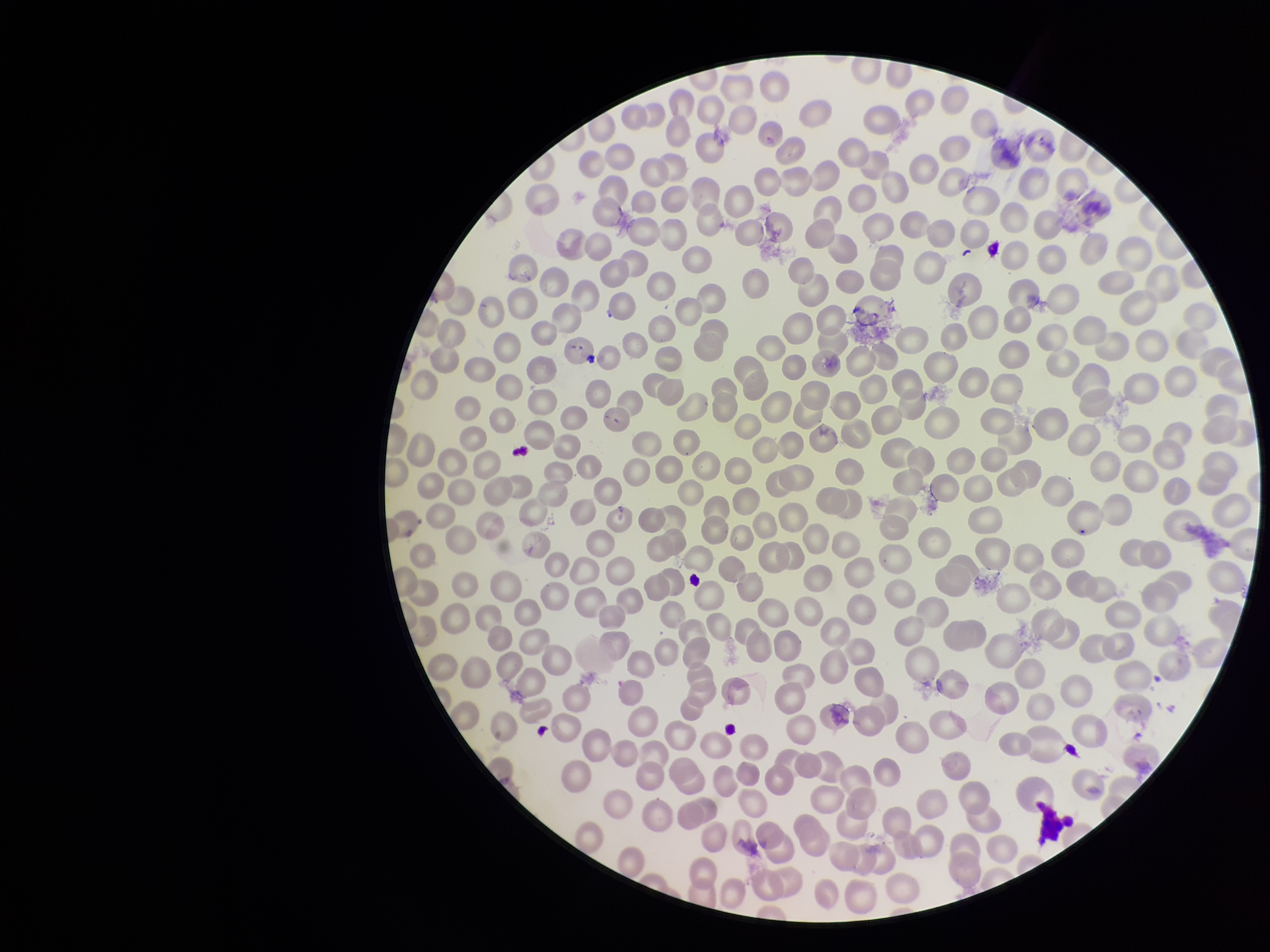 Parasitized red blood cells: none detected. Parasitized red blood cell count: 0. Patient malaria status: infected. One field from this slide. Red blood cell count: 237. Stained with Giemsa. Preparation: thin blood smear. Smartphone photograph taken through the eyepiece of a microscope. Image is 1270×952 pixels. Species reported for this patient: Plasmodium falciparum.